State which cell type is depicted.
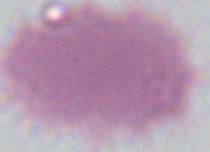

This is an erythrocyte.

Summary:
  - Modality: photomicrograph
  - Magnification: 1000x